Give the position of every leukocyte visible.
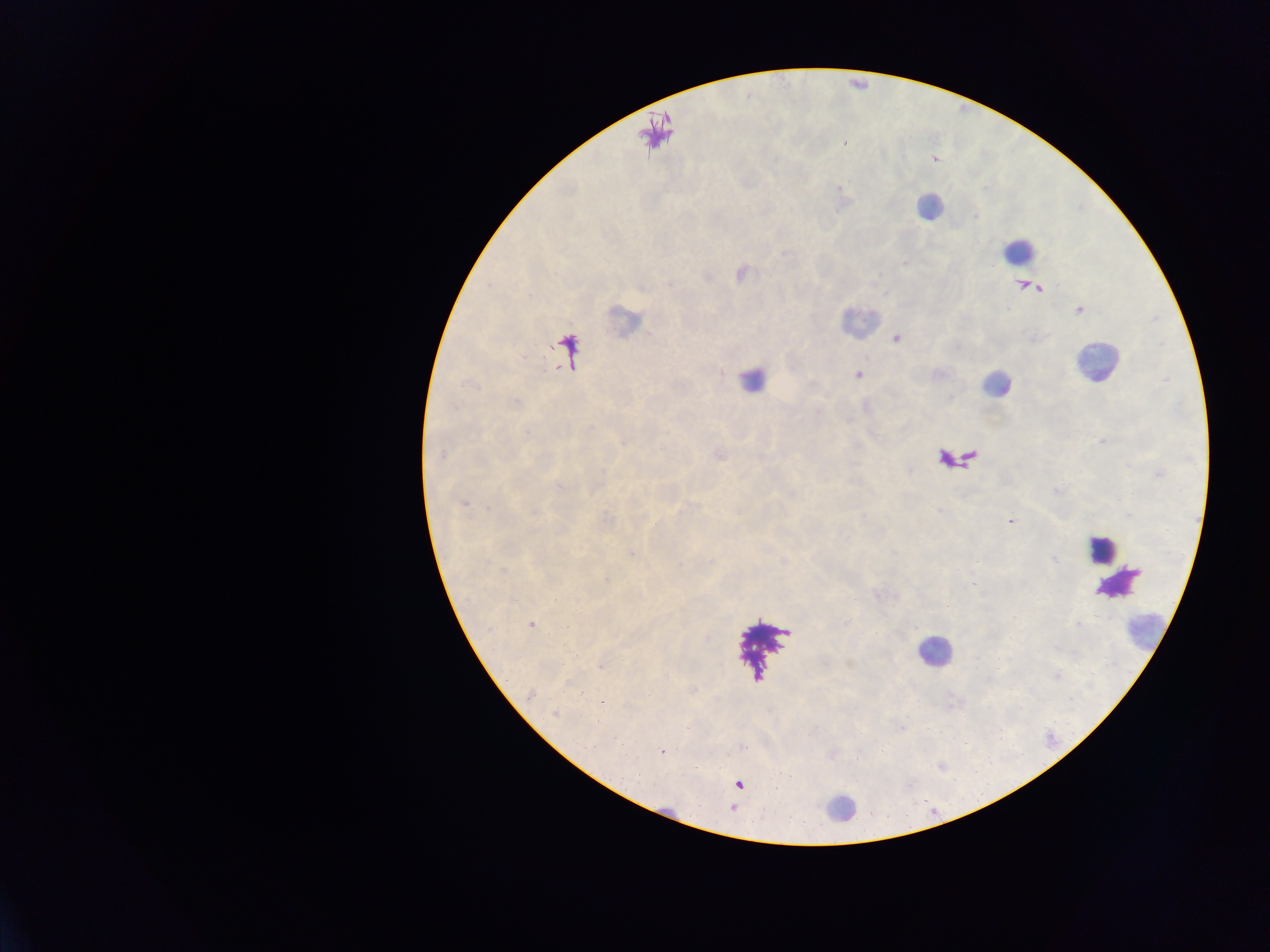

Approximate centers as x y in pixels.
Leukocytes: 930 207; 1018 250; 858 322; 1094 362; 751 382; 996 384; 1100 549; 1145 629; 933 651; 841 808.

field_of_view: single
image_size: 1270×952 pixels
preparation: thick blood film
country: Ghana
plasmodium_parasite_locations: 'approximate centers as x y in pixels: 669 283; 896 341; 858 374; 442 456; 462 504; 1010 521; 655 525; 531 624; 599 667; 530 695; 554 714; 661 752'
capture: mobile-phone photograph through a microscope